Locate every blood parasite and identify its species.
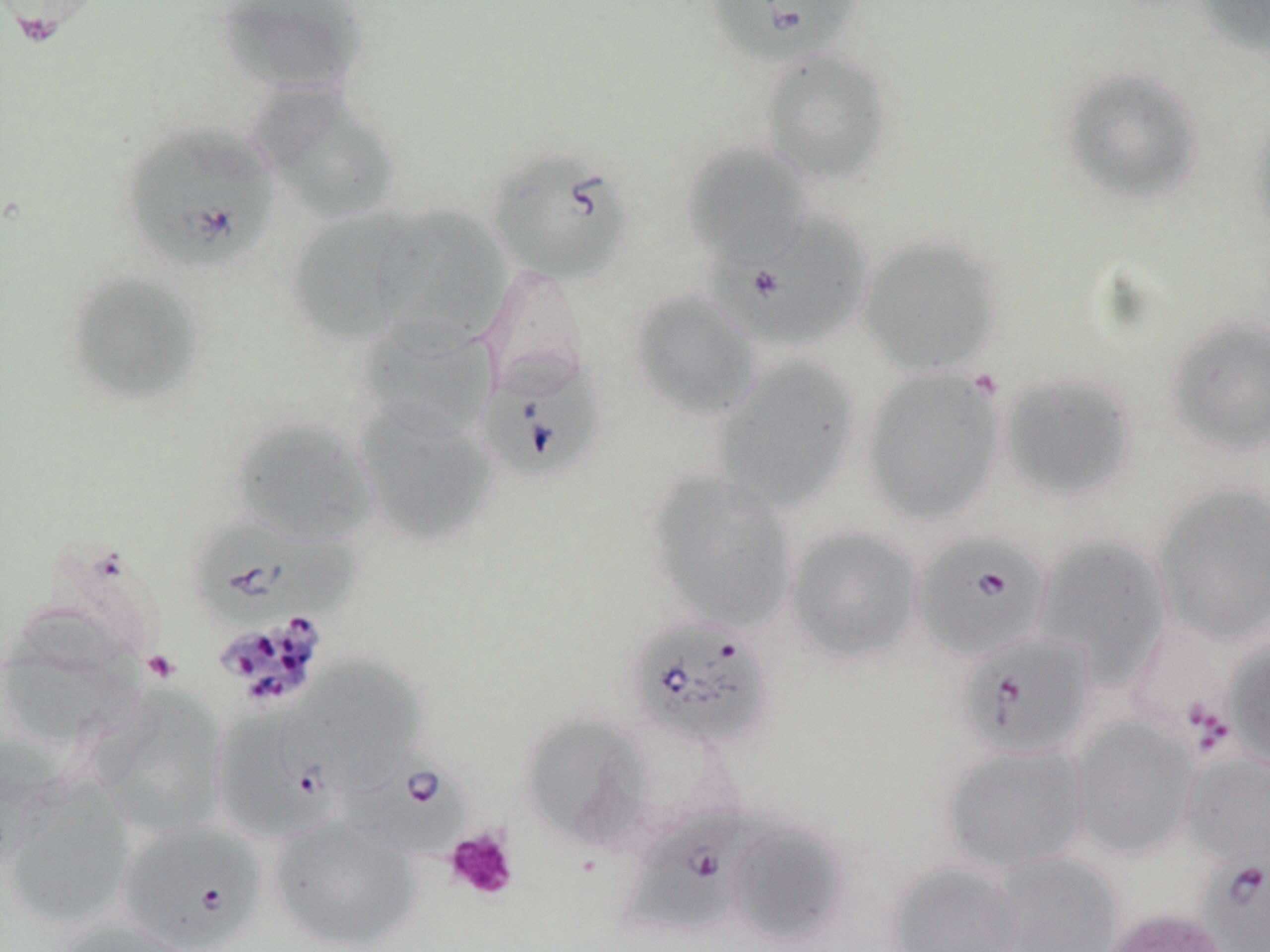
Approximate bounding boxes as [x1, y1, x2, y2] in pixels.
Babesia divergens-infected red blood cells: [705, 0, 862, 67], [121, 123, 280, 274], [486, 146, 634, 286], [711, 211, 875, 352], [476, 351, 605, 482], [191, 516, 353, 636], [913, 530, 1051, 663], [627, 616, 773, 750], [1125, 618, 1239, 754], [957, 629, 1096, 761], [211, 705, 341, 845], [338, 748, 472, 864], [621, 803, 761, 939], [115, 820, 268, 951], [1200, 854, 1270, 951].
No Plasmodium falciparum, Plasmodium ovale, Plasmodium malariae, Plasmodium vivax, or Trypanosoma brucei observed.

slide_level_diagnosis: Babesia divergens
magnification: 1000x
preparation: thin blood film
platelet_locations: 'approximate bounding boxes as [x1, y1, x2, y2] in pixels: [143, 650, 180, 684], [445, 827, 519, 901]'
image_size: 1270×952 pixels
modality: light microscopy
field_of_view: single
uninfected_red_blood_cell_locations: 'approximate bounding boxes as [x1, y1, x2, y2] in pixels: [214, 0, 369, 98], [1196, 0, 1270, 59], [758, 48, 893, 185], [1061, 67, 1204, 206], [251, 84, 403, 226], [1247, 110, 1270, 248], [681, 141, 811, 265], [376, 205, 509, 349], [286, 208, 418, 346], [857, 235, 1003, 377], [479, 262, 591, 392], [62, 269, 206, 410], [627, 287, 762, 421], [1167, 317, 1270, 458], [357, 319, 497, 437], [712, 357, 861, 512], [861, 367, 1005, 526], [997, 372, 1139, 504], [352, 399, 498, 548], [228, 415, 379, 548], [645, 469, 797, 631], [1153, 482, 1270, 646], [784, 525, 924, 665], [1032, 535, 1171, 683], [0, 625, 143, 753], [1225, 637, 1270, 772], [287, 657, 426, 793], [90, 686, 230, 838], [519, 713, 652, 852], [1069, 716, 1200, 861], [0, 734, 63, 876], [940, 742, 1089, 874], [1182, 751, 1270, 870], [2, 779, 136, 930], [268, 814, 420, 951], [727, 820, 848, 947], [985, 852, 1124, 952], [884, 859, 1027, 952], [1099, 906, 1230, 952], [56, 915, 194, 952]'
stain: May-Grünwald-Giemsa